Comment on the morphology of the red blood cells.
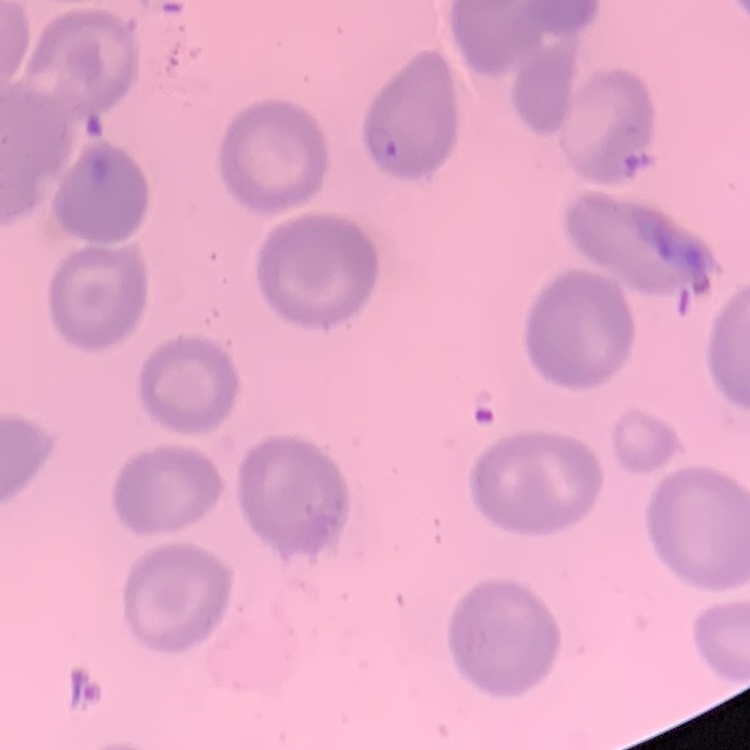
No rouleaux formation.

One tile cut from a larger photomicrograph. Stained with either Field's or Giemsa. Thin blood smear.